Assess the morphology of the red blood cells.
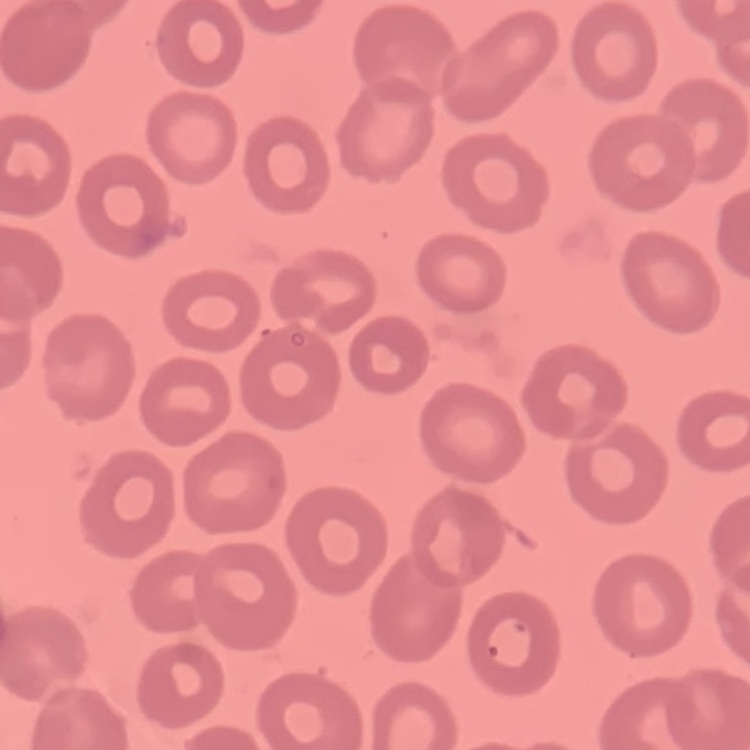

They show no rouleaux formation.

Field's or Giemsa stain. Thin peripheral smear. Square crop of a larger photomicrograph.